Identify the cell.
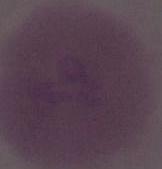

An erythrocyte.

magnification: 1000x
modality: micrograph